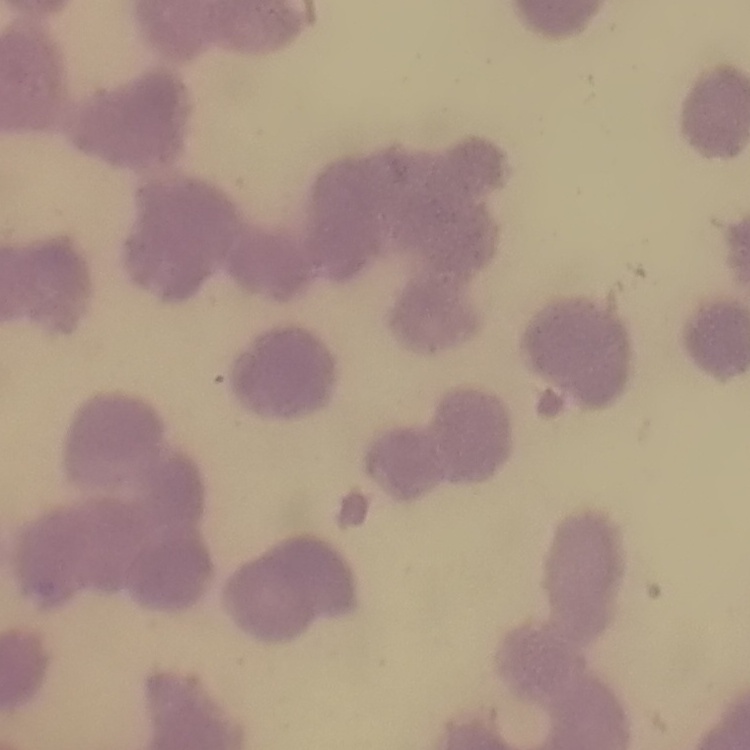
The red blood cells show rouleaux formation. One tile cut from a larger photomicrograph. Stained with either Field's or Giemsa. Thin blood smear.